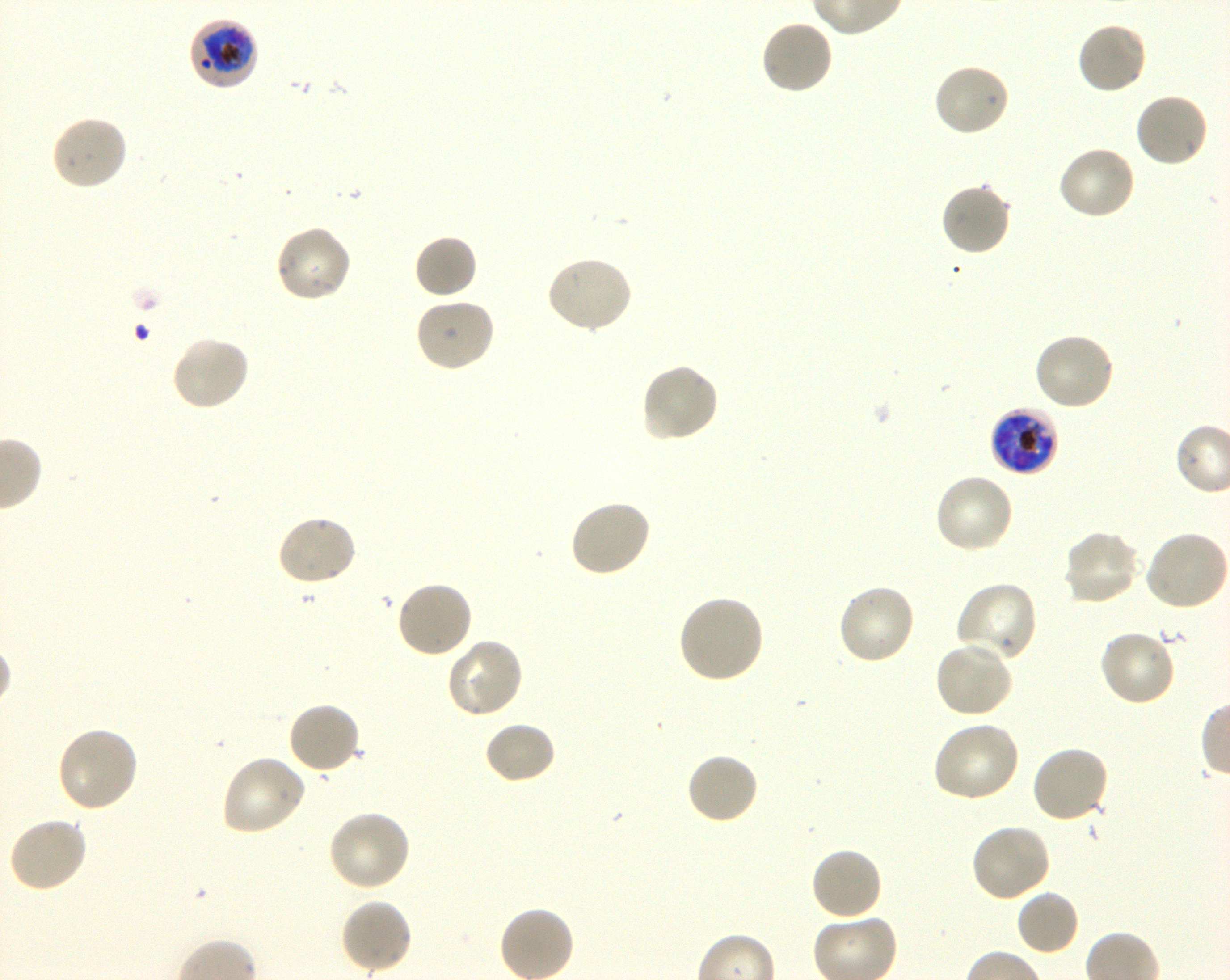

Approximate bounding boxes as (x1, y1, x2, y2) in pixels. Not every red blood cell is marked. A life-cycle stage — or a range of stages, where the recorded stages span more than one — follows each staged infected red blood cell.
Summary:
  - Locations of infected red blood cells: (188, 17, 260, 91) early trophozoite to early schizont; (990, 404, 1057, 477) late trophozoite to late schizont
  - Locations of uninfected red blood cells: (759, 19, 835, 97), (1076, 21, 1149, 96), (932, 63, 1011, 138), (1134, 92, 1210, 169), (50, 114, 129, 191), (1056, 144, 1137, 220), (939, 183, 1012, 257), (274, 224, 354, 304), (413, 234, 478, 300), (545, 255, 634, 335), (413, 298, 497, 373), (1031, 332, 1116, 413), (170, 335, 252, 413), (640, 362, 720, 444), (934, 473, 1015, 555), (568, 498, 653, 578), (275, 514, 358, 588), (1061, 529, 1141, 608), (1144, 531, 1229, 612), (395, 580, 474, 659), (953, 581, 1039, 665), (836, 582, 917, 667), (677, 595, 765, 684), (1097, 629, 1177, 707), (444, 638, 525, 718), (933, 640, 1015, 719), (286, 701, 361, 776), (931, 719, 1021, 804), (484, 722, 556, 785), (55, 725, 140, 813), (1030, 745, 1110, 825), (685, 752, 760, 825), (220, 755, 307, 836), (326, 809, 411, 893), (7, 817, 88, 894), (970, 823, 1053, 904), (809, 846, 884, 923), (1014, 889, 1080, 957), (339, 898, 414, 975)
  - Preparation: thin blood film
  - Field of view: single
  - Culture: Plasmodium falciparum strain 3D7, shaking, in vitro
  - Stain: Giemsa
  - Objective: 100x, oil immersion, numerical aperture 1.30
  - Donor blood group: O+
  - Image size: 1230×980 pixels